Find each parasitized RBC.
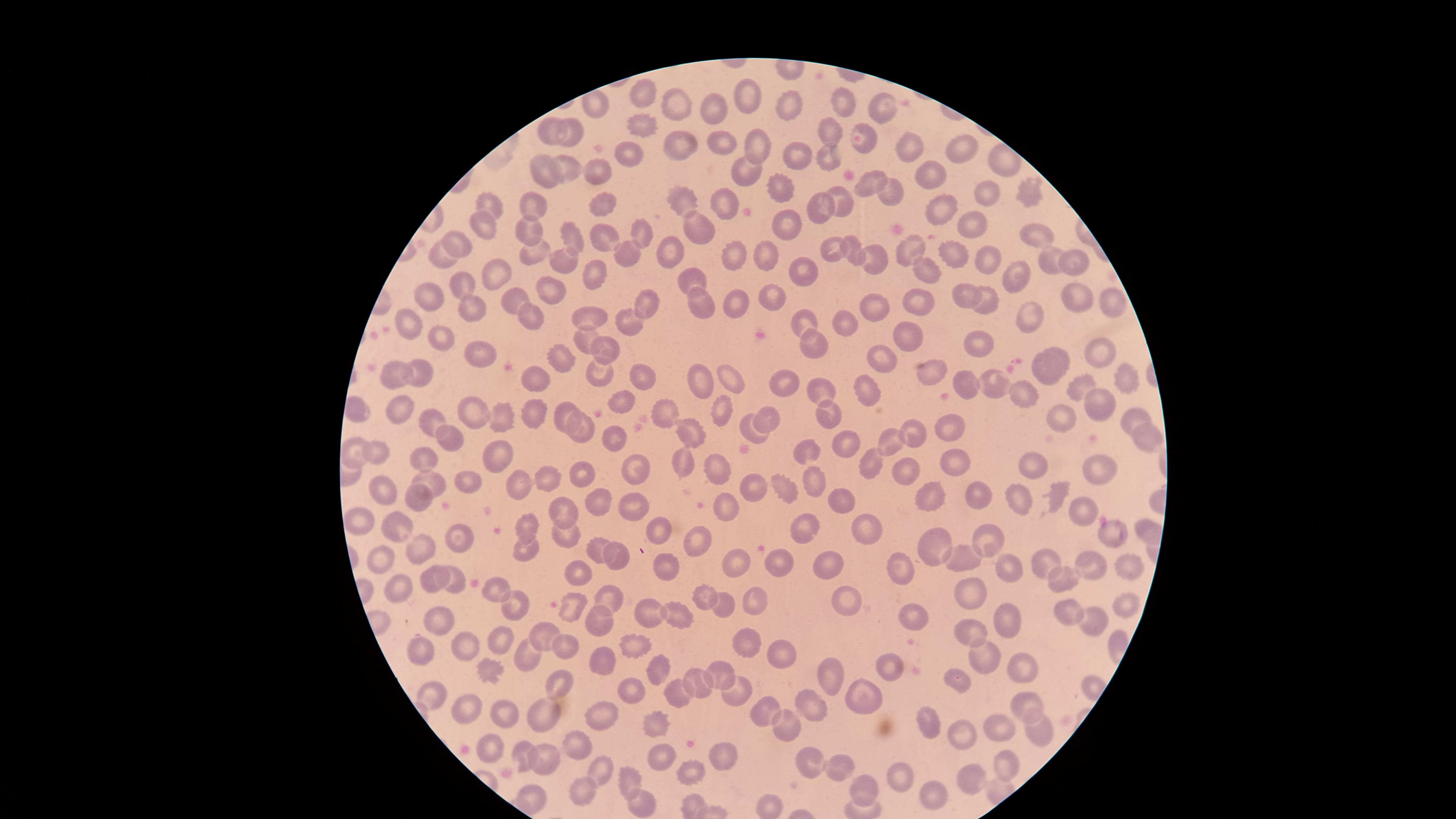
No parasitized RBCs identified.

Approximate marker points as [x, y] in pixels.
Summary:
  - Uninfected RBCs: [643, 95], [749, 99], [839, 102], [679, 103], [790, 103], [881, 103], [599, 106], [715, 106], [641, 130], [541, 131], [832, 133], [571, 135], [719, 141], [864, 142], [673, 145], [754, 148], [906, 148], [959, 149], [826, 155], [632, 156], [797, 159], [596, 164], [564, 168], [542, 171], [746, 171], [936, 175], [866, 184], [891, 189], [1025, 189], [779, 190], [988, 193], [722, 199], [840, 199], [680, 201], [599, 203], [824, 206], [541, 207], [494, 208], [943, 208], [785, 224], [972, 224], [483, 228], [639, 229], [693, 233], [530, 234], [569, 237], [601, 237], [1042, 237], [458, 244], [671, 247], [835, 250], [854, 250], [912, 250], [532, 251], [444, 252], [951, 252], [631, 254], [733, 254], [766, 256], [878, 258], [985, 258], [562, 261], [1072, 262], [1048, 264], [925, 268], [802, 271], [691, 274], [498, 275], [596, 275], [1020, 276], [458, 283], [554, 290], [965, 296], [434, 297], [772, 298], [989, 299], [1074, 299], [511, 302], [699, 302], [1110, 302], [737, 303], [872, 304], [920, 305], [645, 307], [475, 311], [1022, 313], [529, 316], [594, 318], [630, 319], [842, 320], [412, 323], [806, 324], [907, 336], [585, 338], [439, 339], [816, 346], [975, 347], [605, 348], [1102, 354], [881, 355], [1064, 356], [561, 357], [480, 359], [1049, 370], [422, 372], [925, 372], [396, 373], [639, 373], [730, 375], [1120, 376], [600, 377], [701, 379], [965, 379], [539, 381], [875, 384], [995, 385], [786, 386], [1080, 387], [827, 391], [1026, 395], [625, 398], [1100, 403], [723, 408], [662, 411], [537, 412], [469, 413], [397, 414], [1064, 415], [563, 416], [825, 417], [507, 420], [771, 420], [1126, 420], [955, 423], [427, 424], [586, 425], [692, 429], [912, 433], [752, 434], [618, 439], [886, 440], [1151, 440], [451, 442], [849, 443], [374, 449], [497, 450], [804, 450], [355, 453], [423, 454], [1030, 460], [678, 461], [873, 461], [959, 462], [721, 464], [636, 466], [905, 467], [1099, 469], [585, 472], [546, 473], [470, 478], [810, 479], [434, 481], [522, 481], [786, 481], [386, 486], [754, 487], [925, 493], [419, 495], [1060, 497], [844, 500], [977, 500], [593, 501], [1021, 501], [633, 506], [728, 506], [1083, 507], [558, 511], [362, 514], [399, 521], [523, 523], [798, 525], [865, 528], [660, 531], [561, 532], [1112, 533], [461, 534], [993, 536], [937, 541], [699, 544], [423, 545], [521, 545], [597, 551], [620, 554], [386, 556], [738, 560], [1124, 560], [965, 561], [1045, 562], [828, 564], [904, 564], [668, 566], [1008, 567], [780, 568], [1091, 570], [437, 574], [1063, 575], [577, 576], [456, 581], [402, 583], [496, 590], [701, 594], [964, 594], [748, 596], [611, 599], [837, 599], [515, 601], [723, 602], [1122, 604], [645, 610], [571, 612], [1068, 612], [672, 614], [1088, 617], [599, 618], [912, 619], [440, 620], [1010, 620], [971, 632], [544, 633], [500, 636], [567, 642], [630, 645], [757, 645], [427, 646], [468, 647], [785, 651], [526, 653], [982, 655], [608, 658], [893, 661], [827, 666], [490, 668], [662, 669], [1030, 672], [716, 673], [698, 680], [560, 683], [955, 684], [677, 685], [867, 687], [739, 689], [629, 692], [428, 694], [1025, 703], [764, 704], [467, 705], [804, 706], [540, 713], [501, 717], [781, 720], [931, 721], [608, 722], [658, 722], [999, 728], [964, 731], [1036, 733], [491, 743], [573, 743], [519, 752], [725, 753], [545, 754], [662, 757], [1001, 762], [814, 763], [844, 764], [601, 768], [690, 769], [626, 777], [893, 778], [973, 780], [865, 784], [588, 789], [937, 794], [534, 798], [645, 809]
  - Image size: 1456×819 pixels
  - Stain: Giemsa
  - Capture: smartphone photograph through the microscope eyepiece
  - Preparation: thin smear of blood
  - Visible region: circular
  - Field of view: single